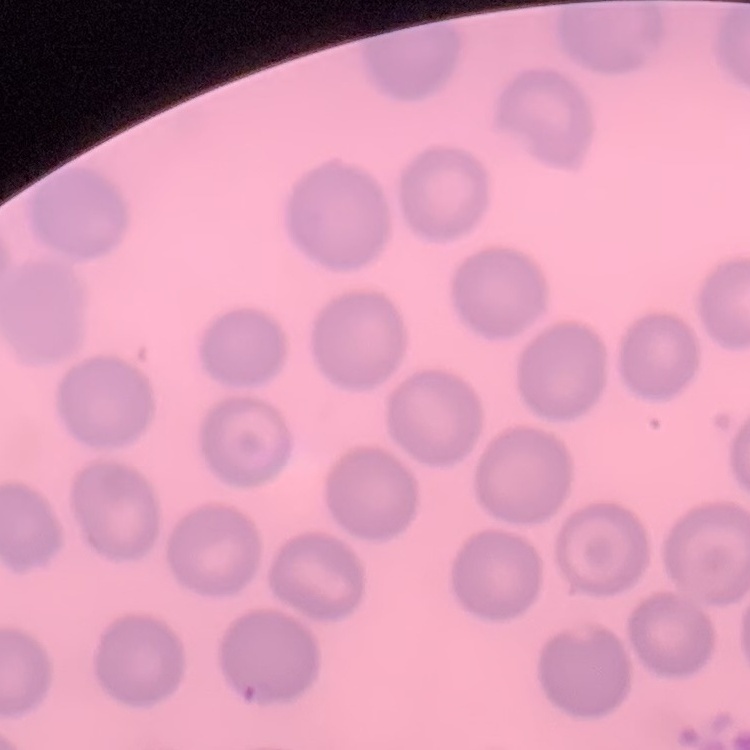
Summary:
  - Red blood cell morphology: no rouleaux formation
  - Stain: Field's or Giemsa
  - Preparation: thin blood smear
  - Image type: square crop of a larger photomicrograph